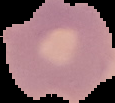

image type = cell region segmented out of the field of view; surrounding area masked to black
malaria status = uninfected
image size = 115×103 pixels
preparation = thin blood smear